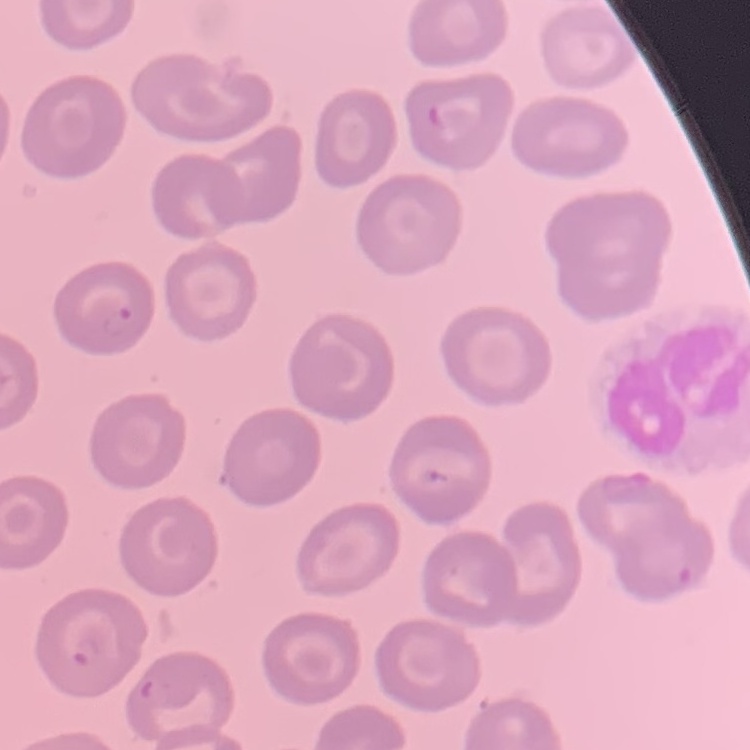
The erythrocytes show no rouleaux formation. Field's or Giemsa stain. Square crop of a larger photomicrograph. Thin blood smear.